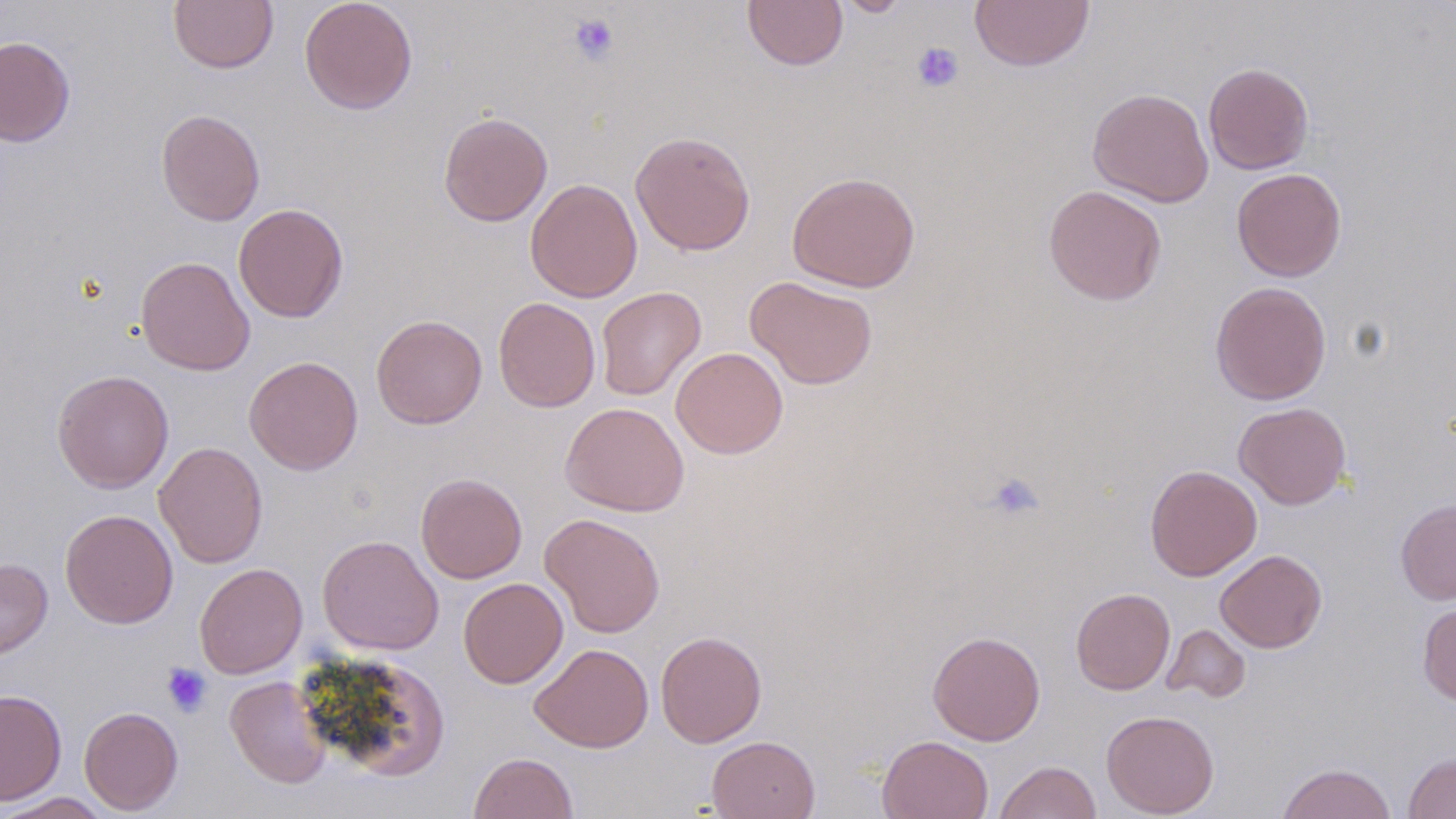

slide-level diagnosis = no evidence of blood parasites
uninfected red blood cell locations = approximate bounding boxes as named x1/y1/x2/y2 corners in pixels: (x1=168, y1=0, x2=279, y2=73), (x1=299, y1=0, x2=418, y2=114), (x1=742, y1=0, x2=848, y2=71), (x1=831, y1=0, x2=914, y2=17), (x1=970, y1=0, x2=1094, y2=71), (x1=0, y1=36, x2=75, y2=147), (x1=1203, y1=62, x2=1314, y2=174), (x1=1087, y1=87, x2=1214, y2=208), (x1=155, y1=108, x2=266, y2=226), (x1=438, y1=111, x2=553, y2=226), (x1=630, y1=130, x2=756, y2=256), (x1=1231, y1=167, x2=1346, y2=282), (x1=786, y1=171, x2=921, y2=293), (x1=525, y1=178, x2=643, y2=303), (x1=1042, y1=185, x2=1167, y2=306), (x1=233, y1=203, x2=349, y2=323), (x1=135, y1=256, x2=255, y2=376), (x1=744, y1=276, x2=878, y2=390), (x1=1210, y1=281, x2=1331, y2=405), (x1=596, y1=286, x2=706, y2=401), (x1=492, y1=296, x2=600, y2=412), (x1=371, y1=315, x2=487, y2=429), (x1=671, y1=347, x2=788, y2=459), (x1=243, y1=356, x2=363, y2=475), (x1=52, y1=369, x2=174, y2=494), (x1=560, y1=402, x2=689, y2=517), (x1=1233, y1=402, x2=1351, y2=510), (x1=153, y1=442, x2=268, y2=568), (x1=1145, y1=464, x2=1262, y2=580), (x1=415, y1=473, x2=528, y2=584), (x1=1395, y1=500, x2=1456, y2=605), (x1=60, y1=508, x2=178, y2=629), (x1=539, y1=513, x2=666, y2=638), (x1=317, y1=534, x2=444, y2=655), (x1=1215, y1=549, x2=1327, y2=653), (x1=0, y1=558, x2=53, y2=661), (x1=194, y1=562, x2=307, y2=678), (x1=458, y1=577, x2=568, y2=689), (x1=1071, y1=588, x2=1175, y2=695), (x1=1418, y1=601, x2=1456, y2=706), (x1=1161, y1=624, x2=1251, y2=703), (x1=655, y1=630, x2=767, y2=748), (x1=927, y1=630, x2=1045, y2=745), (x1=529, y1=643, x2=654, y2=753), (x1=345, y1=663, x2=456, y2=781), (x1=225, y1=676, x2=333, y2=788), (x1=0, y1=688, x2=67, y2=805), (x1=79, y1=706, x2=183, y2=814), (x1=1100, y1=710, x2=1219, y2=817), (x1=706, y1=735, x2=820, y2=818), (x1=877, y1=735, x2=993, y2=819), (x1=1403, y1=751, x2=1456, y2=818), (x1=468, y1=752, x2=579, y2=819), (x1=994, y1=760, x2=1102, y2=819), (x1=1276, y1=762, x2=1397, y2=819), (x1=1, y1=792, x2=114, y2=819)
magnification = 1000x
preparation = thin blood film
image size = 1456×819 pixels
stain = May-Grünwald-Giemsa
modality = optical microscopy
platelet locations = approximate bounding boxes as named x1/y1/x2/y2 corners in pixels: (x1=568, y1=13, x2=619, y2=65), (x1=911, y1=42, x2=964, y2=93), (x1=986, y1=471, x2=1046, y2=522), (x1=162, y1=663, x2=212, y2=717)
field of view = one of a larger specimen